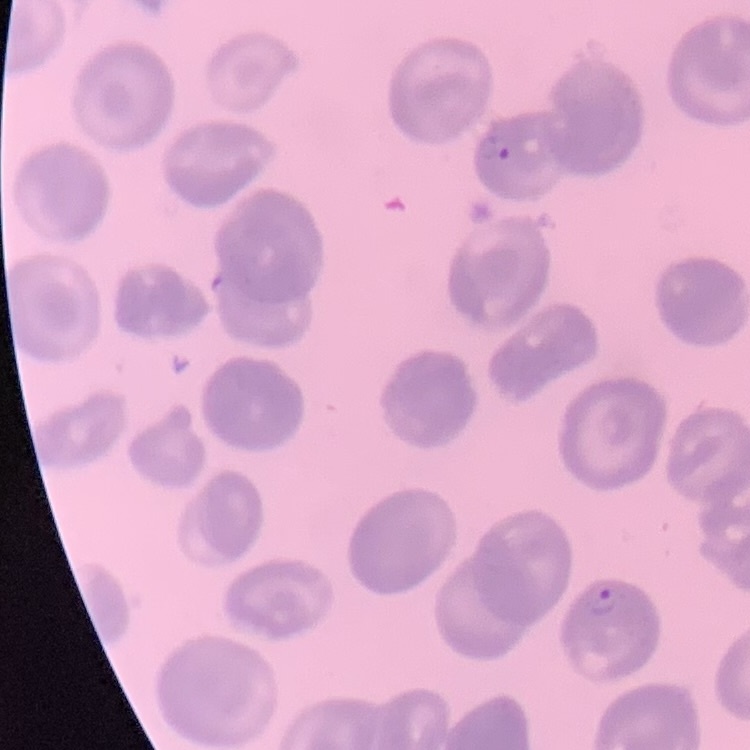 The erythrocytes exhibit no rouleaux formation. Thin blood smear. One tile cut from a larger photomicrograph. Stained with either Field's or Giemsa.